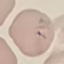
Result: malaria parasites identified. Acquired by smartphone through the microscope eyepiece. Giemsa-stained preparation. Thin smear of blood. Automatically extracted cell patch, resized to 64 × 64 pixels.